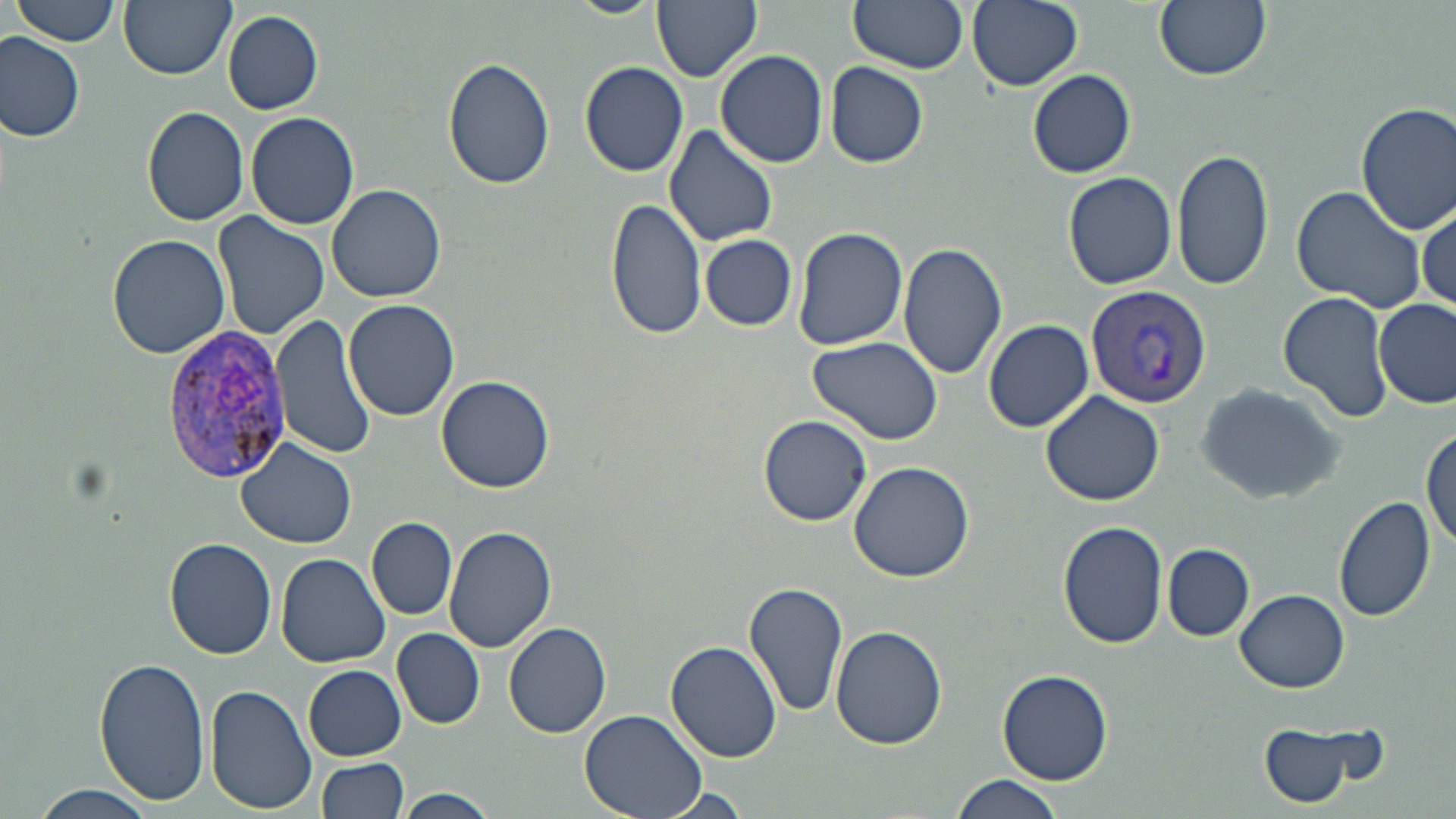
plasmodium_vivax_infected_red_blood_cell_locations: 'approximate bounding boxes as [x1, y1, x2, y2] in pixels: [1085, 286, 1210, 409], [160, 327, 295, 480]'
slide_level_diagnosis: Plasmodium vivax
magnification: 1000x
uninfected_red_blood_cell_locations: 'approximate bounding boxes as [x1, y1, x2, y2] in pixels: [12, 0, 122, 46], [118, 0, 234, 80], [567, 0, 664, 18], [653, 0, 762, 83], [847, 0, 968, 75], [967, 0, 1082, 90], [1153, 0, 1271, 81], [223, 10, 323, 114], [0, 33, 86, 142], [715, 49, 829, 168], [442, 58, 556, 190], [579, 62, 688, 177], [825, 62, 930, 167], [1028, 69, 1136, 178], [1355, 102, 1456, 233], [141, 105, 250, 227], [247, 110, 360, 230], [663, 122, 778, 247], [1174, 147, 1273, 292], [1063, 171, 1176, 288], [327, 183, 447, 303], [1291, 184, 1428, 316], [606, 196, 707, 342], [1416, 201, 1454, 314], [212, 212, 330, 340], [792, 226, 909, 350], [108, 234, 230, 358], [700, 235, 796, 330], [897, 240, 1009, 380], [1280, 294, 1390, 421], [343, 299, 461, 422], [1373, 299, 1455, 407], [272, 312, 377, 462], [984, 319, 1093, 432], [808, 336, 944, 446], [436, 375, 557, 493], [1193, 380, 1349, 504], [1040, 391, 1168, 508], [757, 414, 872, 527], [1420, 429, 1454, 555], [236, 437, 360, 548], [847, 460, 973, 581], [1333, 495, 1436, 623], [367, 515, 457, 619], [1059, 521, 1170, 648], [443, 522, 559, 653], [165, 539, 278, 660], [1163, 544, 1254, 639], [277, 554, 390, 669], [744, 579, 849, 720], [1234, 588, 1349, 692], [503, 618, 611, 739], [830, 624, 947, 752], [393, 628, 485, 728], [666, 639, 782, 763], [95, 656, 211, 806], [303, 665, 406, 760], [997, 668, 1113, 786], [205, 684, 317, 814], [579, 708, 706, 818], [1253, 717, 1387, 810], [316, 757, 409, 818], [950, 774, 1066, 819], [29, 784, 158, 818], [397, 788, 495, 819]'
image_size: 1456×819 pixels
field_of_view: one of a larger specimen
stain: May-Grünwald-Giemsa
preparation: thin blood film
modality: light microscopy